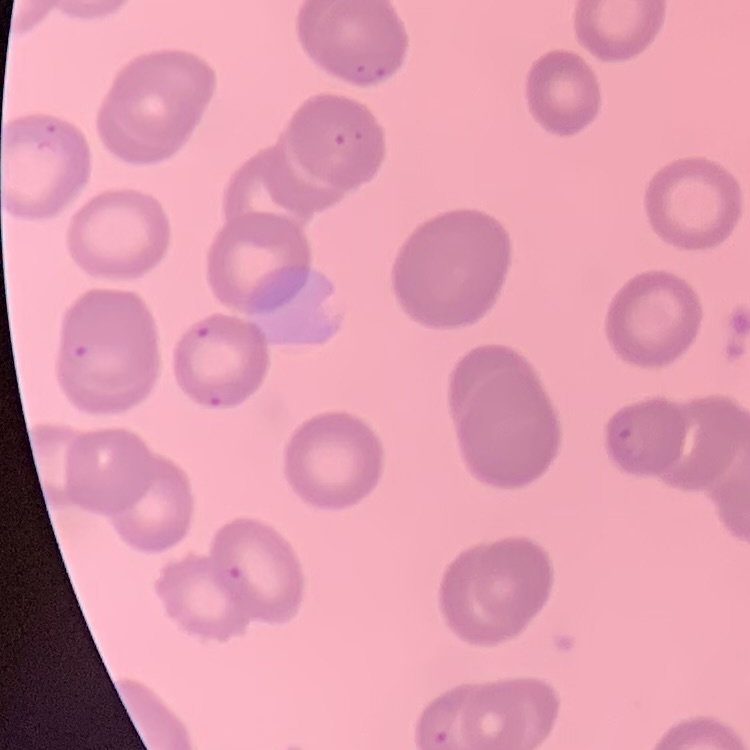

The red blood cells show no rouleaux formation. One tile cut from a larger photomicrograph. Thin blood smear. Stained with either Field's or Giemsa.